Give the position of every leukocyte visible.
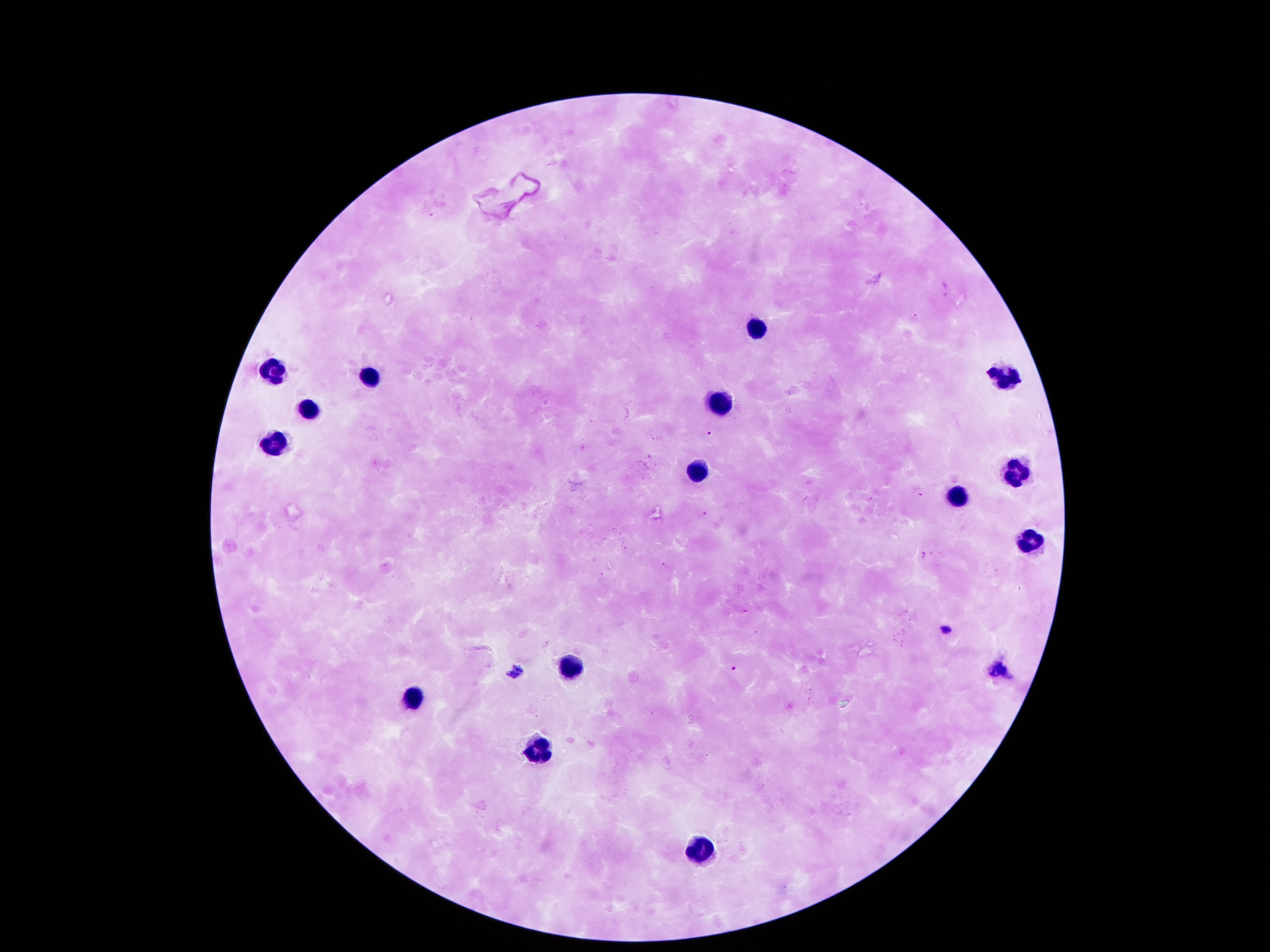

Approximate centers as {x, y} in pixels.
Leukocytes: {756, 327}, {272, 372}, {1002, 372}, {366, 375}, {719, 399}, {306, 409}, {269, 445}, {692, 473}, {1012, 475}, {955, 499}, {1032, 543}, {565, 661}, {420, 697}, {535, 747}, {699, 849}.

Summary:
  - Field of view: one from this slide
  - Image size: 1270×952 pixels
  - Stain: Giemsa
  - Magnification: 100x
  - Preparation: thick blood film
  - Capture: smartphone camera through the microscope eyepiece
  - Patient malaria status: not infected